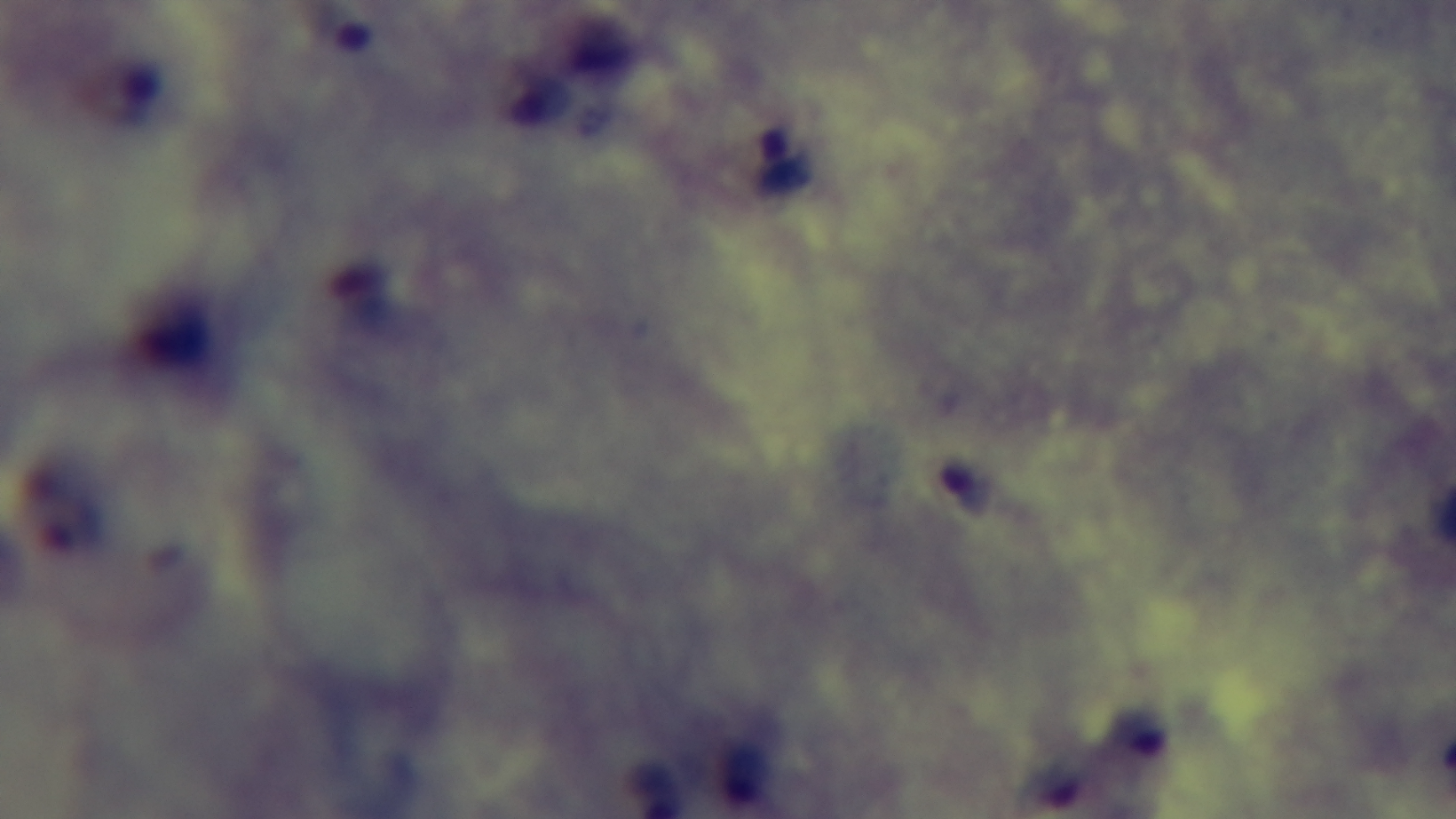
Summary:
  - Objective: 100x oil immersion
  - Stain: Giemsa
  - Field of view: single
  - Capture: mounted 4K digital camera
  - Malaria status: positive
  - Preparation: thick blood film
  - Modality: light microscopy